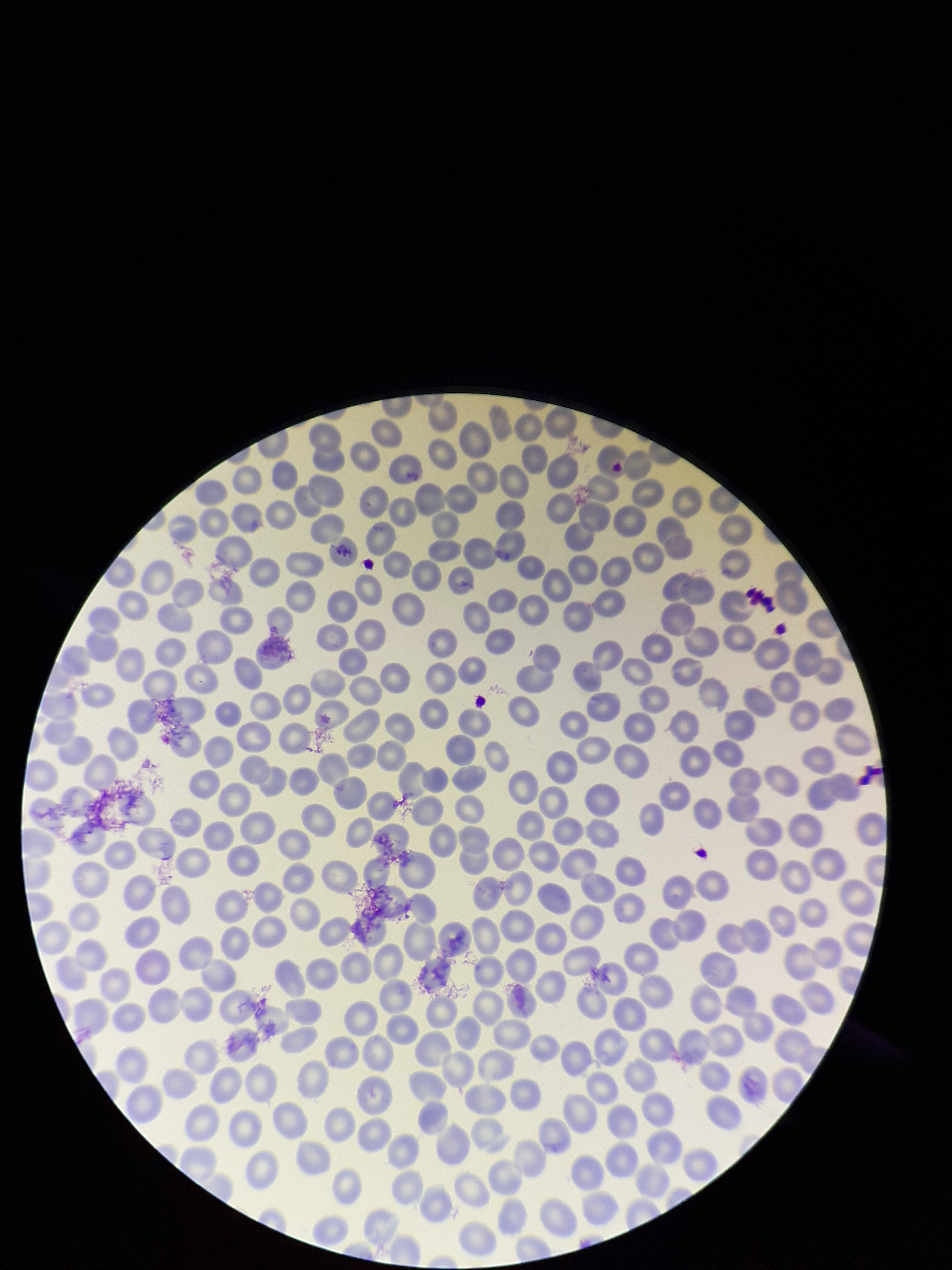
Smartphone photograph taken through the eyepiece of a microscope. Preparation: thin. Stained with Giemsa. Red blood cell count: 239. Single field of view. Patient malaria status: negative. Parasitized red blood cell count: 0. Parasitized red blood cells: none detected. Image is 952×1270 pixels.